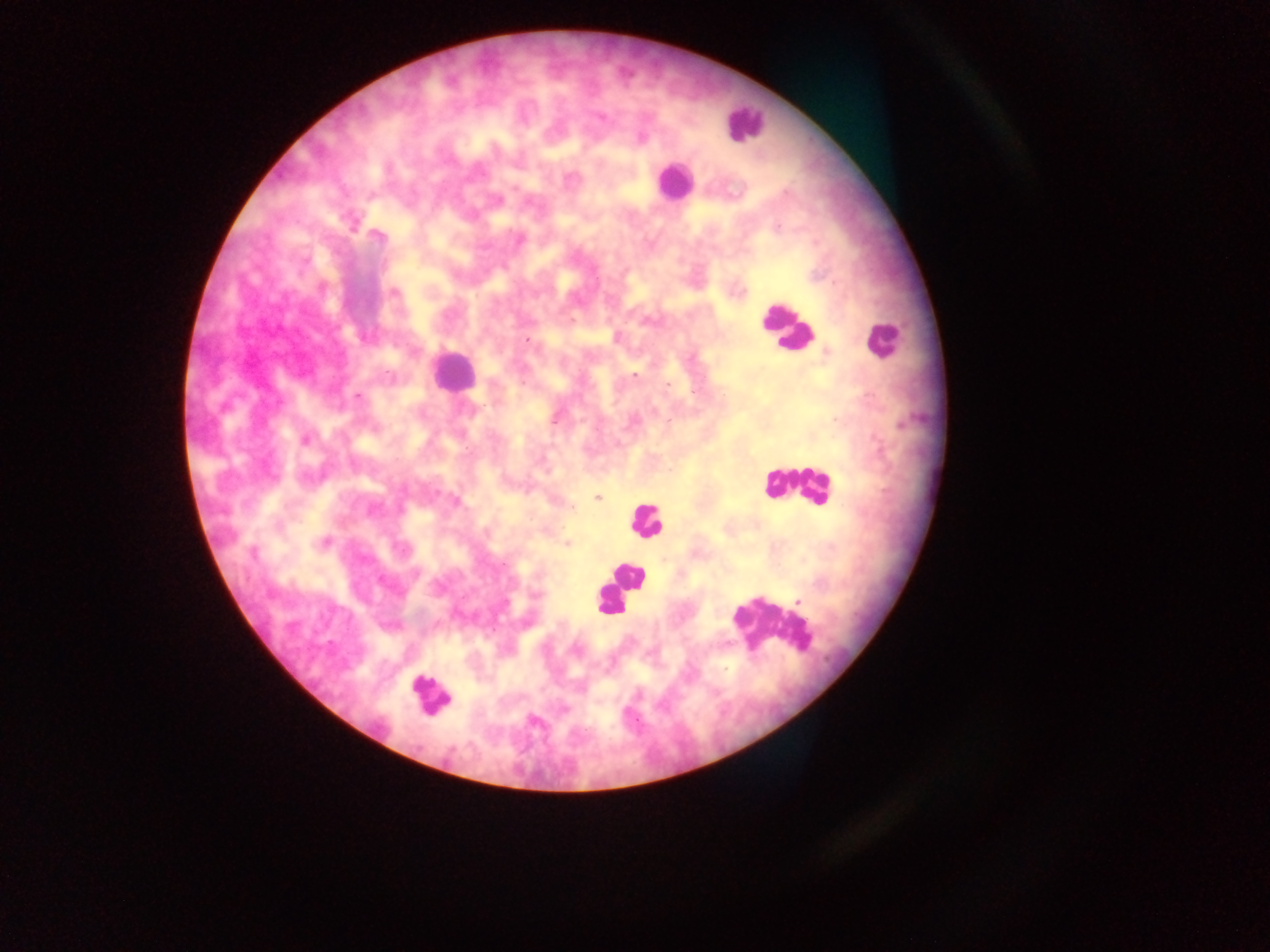

Approximate centers as (x, y) in pixels.
Summary:
  - Leukocyte locations: (742, 123), (672, 181), (787, 328), (881, 340), (449, 370), (796, 485), (645, 519), (627, 575), (618, 588), (609, 600), (767, 626), (429, 696)
  - Malaria parasite locations: (601, 119), (378, 237), (520, 239), (394, 293), (527, 340), (634, 376), (358, 396), (556, 419), (305, 440), (597, 498), (456, 501), (325, 541), (568, 544), (253, 552), (415, 573)
  - Capture: mobile-phone photograph through a microscope
  - Field of view: single
  - Country: Ghana
  - Preparation: thick blood smear
  - Image size: 1270×952 pixels